Find each parasitized red blood cell.
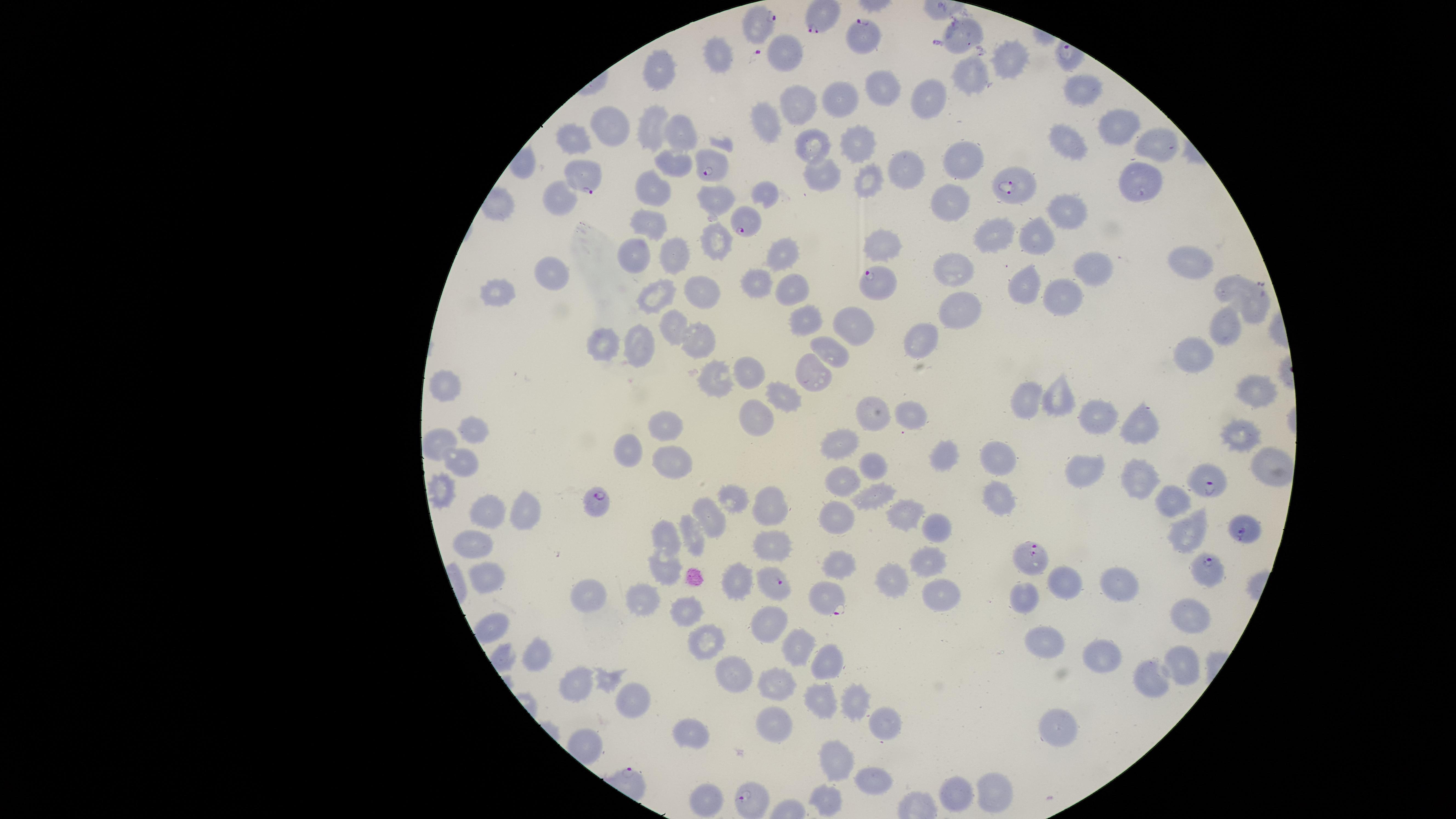

Approximate marker points as (x, y) in pixels.
Parasitized red blood cells: (821, 17), (757, 24), (860, 41), (711, 162), (583, 176), (1012, 185), (745, 222), (873, 282), (1208, 482), (597, 504), (1244, 530), (1030, 558), (1206, 568), (777, 582), (824, 598), (746, 798).

field of view = single
species = Plasmodium falciparum
preparation = thin blood smear
image size = 1456×819 pixels
stain = Giemsa
capture = smartphone photograph through the microscope eyepiece
uninfected red blood cells = approximate marker points as (x, y) in pixels: (789, 49), (719, 57), (1002, 61), (654, 73), (966, 78), (874, 85), (1083, 90), (933, 94), (844, 95), (798, 106), (769, 116), (619, 123), (650, 123), (681, 124), (1118, 124), (577, 133), (858, 139), (1071, 143), (813, 144), (1150, 146), (962, 154), (669, 159), (906, 166), (819, 173), (865, 177), (1141, 178), (655, 184), (764, 192), (710, 197), (955, 198), (560, 205), (1068, 209), (649, 223), (993, 231), (1036, 235), (716, 242), (882, 242), (641, 254), (681, 255), (781, 257), (1190, 260), (1089, 264), (955, 269), (548, 278), (756, 285), (1230, 285), (1025, 287), (790, 290), (702, 291), (497, 294), (652, 297), (1060, 300), (961, 307), (1255, 313), (804, 315), (854, 322), (664, 327), (1223, 329), (701, 341), (606, 343), (924, 346), (636, 347), (833, 350), (1194, 354), (748, 367), (815, 374), (720, 378), (450, 389), (1252, 389), (1056, 400), (780, 403), (1027, 404), (873, 411), (909, 415), (1100, 416), (1141, 418), (760, 419), (665, 423), (475, 430), (1241, 435), (440, 441), (843, 442), (628, 448), (670, 453), (940, 454), (1003, 458), (1261, 460), (875, 463), (461, 467), (1089, 472), (840, 475), (1144, 481), (440, 490), (870, 493), (738, 494), (1005, 495), (1177, 502), (770, 506), (484, 507), (513, 508), (899, 510), (710, 517), (838, 523), (930, 529), (1188, 530), (692, 534), (666, 535), (473, 537), (771, 541), (923, 560), (841, 567), (665, 568), (739, 577), (484, 578), (894, 579), (1061, 580), (1118, 586), (944, 592), (647, 599), (590, 601), (1022, 604), (687, 612), (1190, 620), (766, 623), (497, 631), (706, 637), (800, 648), (1043, 648), (1096, 654), (537, 656), (834, 658), (730, 669), (1181, 669), (1150, 676), (781, 681), (578, 685), (815, 696), (856, 702), (636, 706), (773, 722), (884, 727), (1053, 729), (696, 735), (846, 758), (874, 778), (957, 791), (994, 793), (705, 798), (830, 801)
visible region = circular